Point out each Plasmodium parasite.
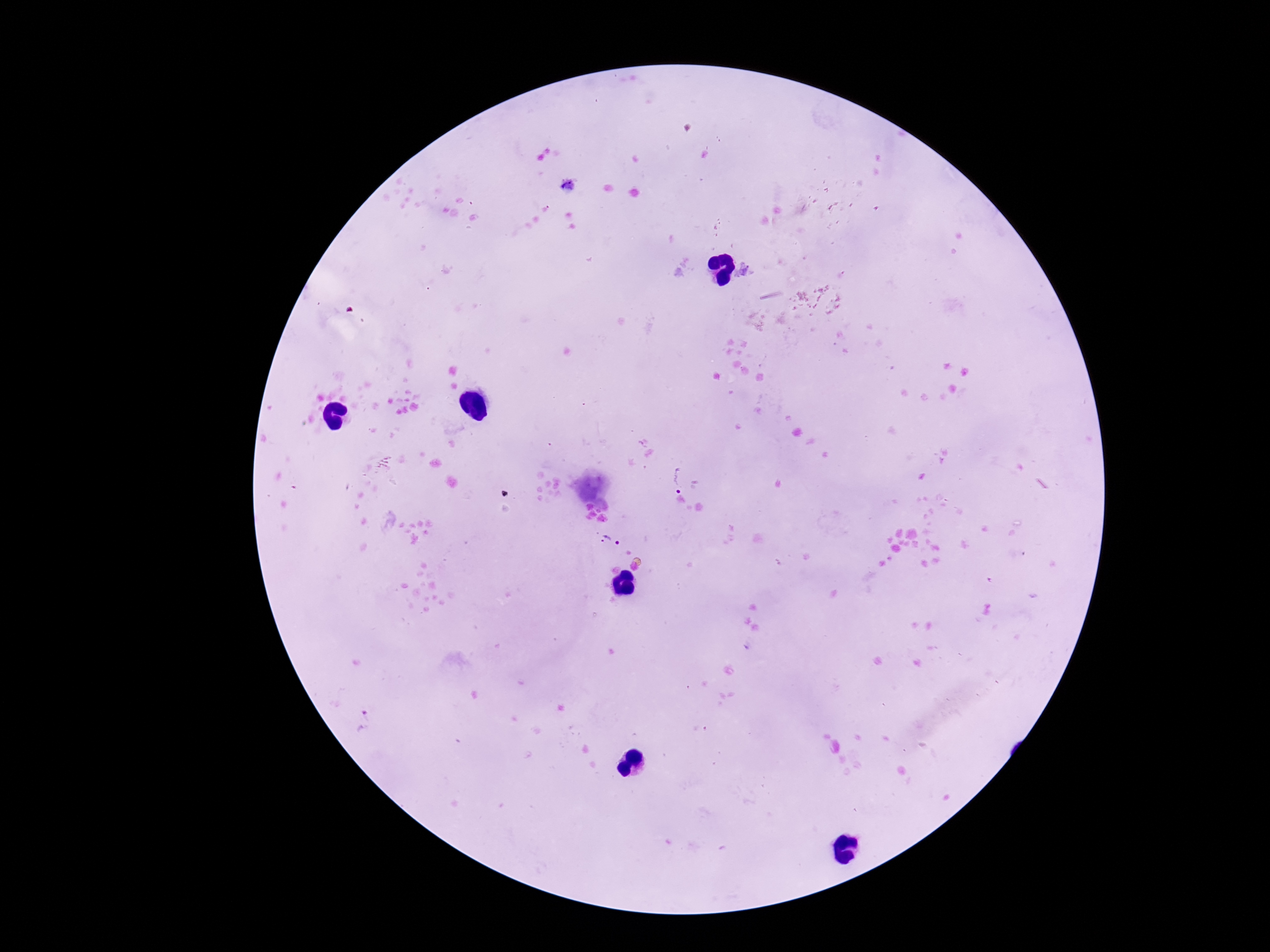
Approximate centers as {x, y} in pixels.
Plasmodium parasites: {569, 187}, {675, 476}, {609, 542}.

Thick blood smear. 100x magnification. Patient malaria status: infected. Smartphone photograph taken through the microscope eyepiece. Giemsa stain. Single field of view. Image is 1270×952 pixels.